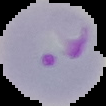
Summary:
  - Image size: 106×106 pixels
  - Image type: cell region segmented out of the field of view; surrounding area masked to black
  - Preparation: thin blood smear
  - Result: Plasmodium parasites identified